Classify this cell by malaria status.
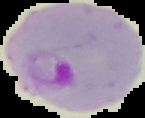

Parasitized.

Summary:
  - Image type: segmented cell region with the area outside set to black
  - Image size: 145×118 pixels
  - Preparation: thin blood film